Report the malaria status of this cell.
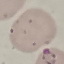

It is parasitized.

Summary:
  - Preparation: thin smear
  - Capture: smartphone camera at the microscope eyepiece
  - Stain: Giemsa
  - Image type: automatically extracted cell patch, resized to 64 × 64 pixels